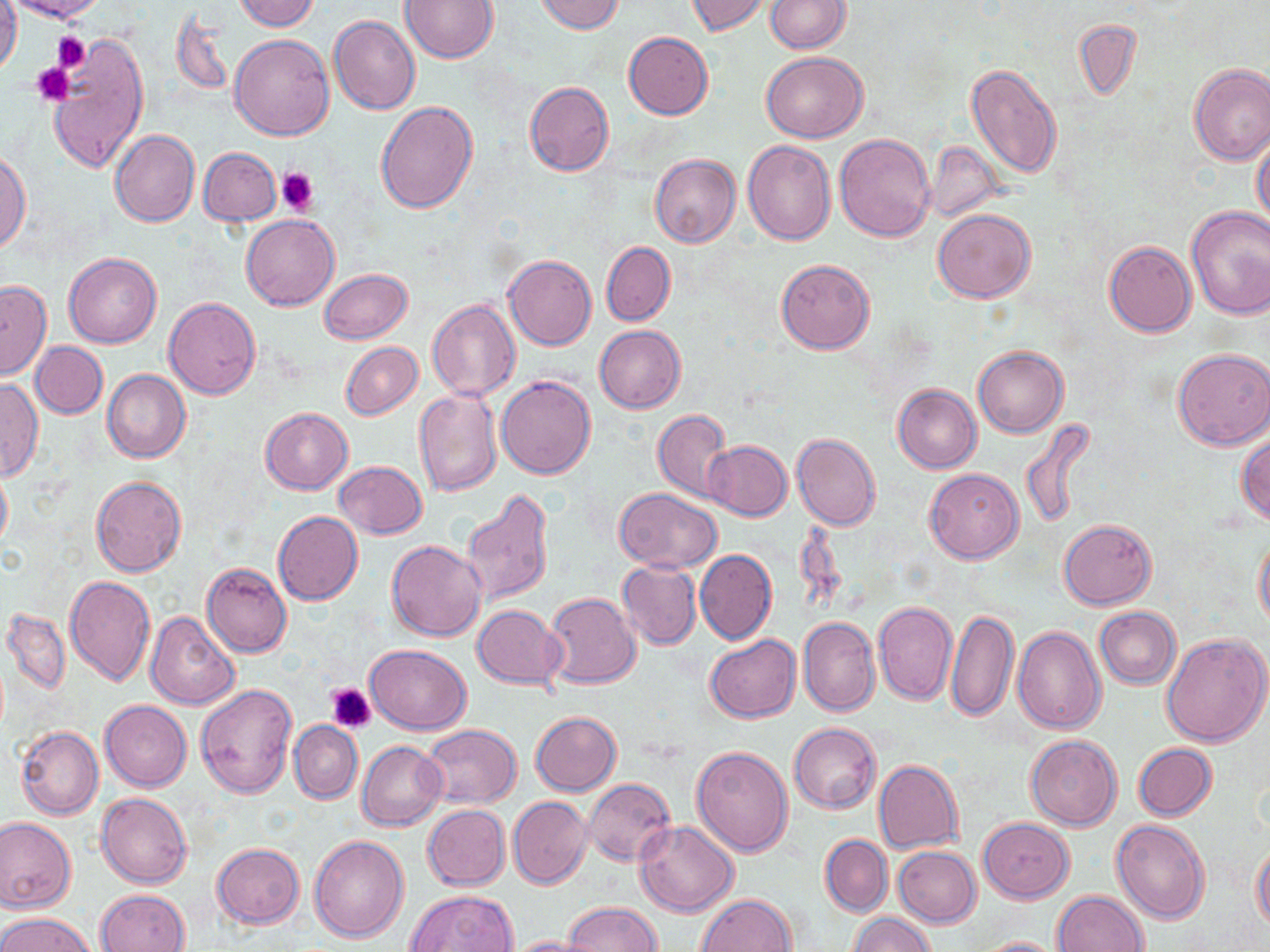 Approximate bounding boxes as named x1/y1/x2/y2 corners in pixels. Platelet locations: (x1=52, y1=32, x2=92, y2=72), (x1=31, y1=61, x2=75, y2=107), (x1=275, y1=167, x2=318, y2=215), (x1=327, y1=682, x2=376, y2=733). Uninfected red blood cell locations: (x1=0, y1=0, x2=22, y2=78), (x1=6, y1=0, x2=109, y2=23), (x1=233, y1=0, x2=319, y2=31), (x1=533, y1=0, x2=627, y2=34), (x1=685, y1=0, x2=770, y2=36), (x1=765, y1=0, x2=849, y2=53), (x1=402, y1=1, x2=497, y2=63), (x1=172, y1=14, x2=233, y2=96), (x1=329, y1=16, x2=420, y2=116), (x1=1073, y1=20, x2=1142, y2=102), (x1=229, y1=33, x2=334, y2=141), (x1=624, y1=33, x2=713, y2=119), (x1=45, y1=37, x2=150, y2=173), (x1=342, y1=48, x2=448, y2=177), (x1=760, y1=52, x2=867, y2=143), (x1=965, y1=63, x2=1062, y2=180), (x1=1187, y1=64, x2=1270, y2=165), (x1=525, y1=82, x2=614, y2=177), (x1=375, y1=102, x2=478, y2=213), (x1=110, y1=131, x2=200, y2=227), (x1=835, y1=132, x2=935, y2=241), (x1=1251, y1=132, x2=1270, y2=227), (x1=924, y1=140, x2=1007, y2=220), (x1=742, y1=141, x2=836, y2=246), (x1=199, y1=147, x2=281, y2=226), (x1=0, y1=150, x2=31, y2=253), (x1=649, y1=155, x2=740, y2=248), (x1=1186, y1=207, x2=1270, y2=319), (x1=933, y1=208, x2=1036, y2=303), (x1=242, y1=215, x2=338, y2=312), (x1=1104, y1=239, x2=1197, y2=337), (x1=602, y1=241, x2=675, y2=325), (x1=64, y1=252, x2=162, y2=348), (x1=503, y1=254, x2=596, y2=351), (x1=775, y1=259, x2=875, y2=353), (x1=318, y1=269, x2=412, y2=344), (x1=0, y1=281, x2=51, y2=378), (x1=164, y1=297, x2=260, y2=399), (x1=426, y1=300, x2=521, y2=402), (x1=595, y1=326, x2=685, y2=413), (x1=31, y1=341, x2=107, y2=418), (x1=341, y1=341, x2=422, y2=421), (x1=973, y1=346, x2=1068, y2=438), (x1=1173, y1=348, x2=1270, y2=450), (x1=102, y1=369, x2=190, y2=464), (x1=497, y1=375, x2=595, y2=478), (x1=0, y1=378, x2=44, y2=482), (x1=892, y1=383, x2=982, y2=473), (x1=413, y1=389, x2=502, y2=497), (x1=259, y1=407, x2=353, y2=494), (x1=653, y1=409, x2=733, y2=503), (x1=1021, y1=419, x2=1096, y2=529), (x1=792, y1=433, x2=881, y2=530), (x1=1236, y1=433, x2=1270, y2=527), (x1=704, y1=440, x2=792, y2=521), (x1=333, y1=461, x2=428, y2=539), (x1=0, y1=464, x2=12, y2=552), (x1=924, y1=468, x2=1023, y2=564), (x1=90, y1=476, x2=187, y2=577), (x1=461, y1=488, x2=554, y2=606), (x1=614, y1=488, x2=722, y2=572), (x1=273, y1=511, x2=363, y2=606), (x1=1058, y1=519, x2=1157, y2=609), (x1=1254, y1=533, x2=1270, y2=632), (x1=387, y1=540, x2=488, y2=642), (x1=695, y1=549, x2=777, y2=644), (x1=201, y1=561, x2=292, y2=657), (x1=617, y1=561, x2=701, y2=650), (x1=64, y1=576, x2=154, y2=686), (x1=543, y1=591, x2=642, y2=689), (x1=874, y1=602, x2=958, y2=705), (x1=472, y1=605, x2=566, y2=689), (x1=947, y1=607, x2=1018, y2=724), (x1=1095, y1=607, x2=1181, y2=688), (x1=2, y1=609, x2=70, y2=694), (x1=147, y1=612, x2=240, y2=711), (x1=797, y1=616, x2=879, y2=717), (x1=1013, y1=626, x2=1105, y2=733), (x1=1161, y1=633, x2=1270, y2=747), (x1=705, y1=634, x2=801, y2=722), (x1=364, y1=644, x2=472, y2=734), (x1=195, y1=683, x2=298, y2=797), (x1=100, y1=700, x2=191, y2=791), (x1=531, y1=712, x2=621, y2=796), (x1=289, y1=720, x2=363, y2=804), (x1=419, y1=723, x2=522, y2=808), (x1=788, y1=723, x2=881, y2=813), (x1=15, y1=727, x2=103, y2=820), (x1=1026, y1=735, x2=1122, y2=830), (x1=357, y1=740, x2=447, y2=831), (x1=1134, y1=744, x2=1216, y2=820), (x1=691, y1=745, x2=793, y2=857), (x1=874, y1=759, x2=964, y2=854), (x1=583, y1=778, x2=676, y2=866), (x1=96, y1=792, x2=192, y2=888), (x1=509, y1=797, x2=591, y2=889), (x1=422, y1=805, x2=509, y2=890), (x1=0, y1=817, x2=76, y2=912), (x1=979, y1=818, x2=1073, y2=902), (x1=1110, y1=818, x2=1211, y2=924), (x1=633, y1=821, x2=740, y2=917), (x1=819, y1=834, x2=892, y2=917), (x1=308, y1=835, x2=409, y2=942), (x1=1252, y1=841, x2=1270, y2=932), (x1=212, y1=842, x2=304, y2=928), (x1=894, y1=847, x2=981, y2=926), (x1=97, y1=888, x2=190, y2=952), (x1=406, y1=889, x2=519, y2=952), (x1=1054, y1=890, x2=1150, y2=952), (x1=696, y1=893, x2=797, y2=952), (x1=565, y1=901, x2=660, y2=952), (x1=0, y1=912, x2=96, y2=952), (x1=850, y1=912, x2=935, y2=952), (x1=503, y1=935, x2=599, y2=952), (x1=968, y1=936, x2=1069, y2=952). Slide-level diagnosis: no evidence of blood parasites. May-Grünwald-Giemsa stain. Optical microscopy. 1000x magnification. Image is 1270×952 pixels. Thin blood smear. One field of a larger specimen.